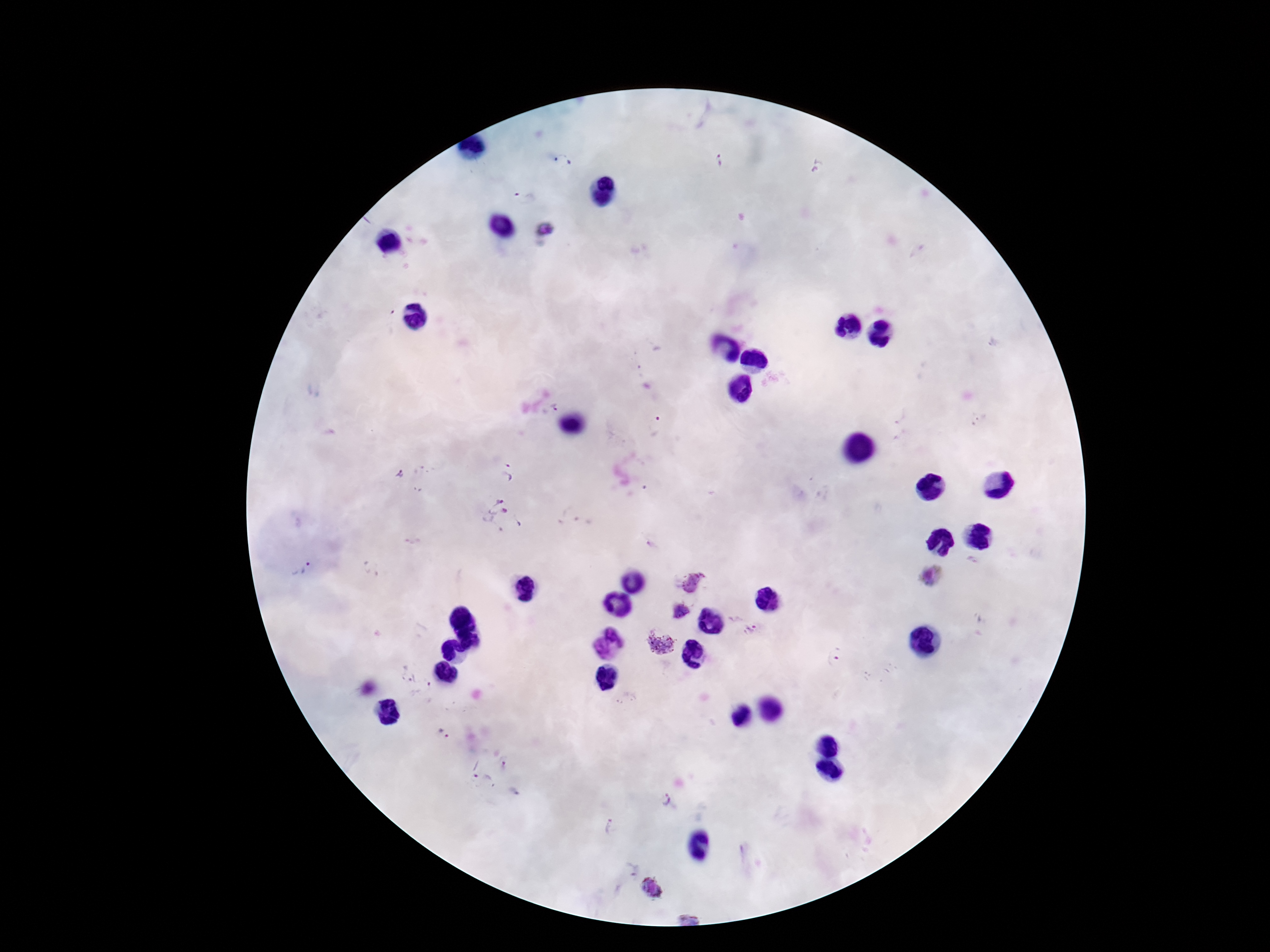
field of view = one from this slide
Plasmodium parasite locations = approximate centers as (x, y) in pixels: (563, 160), (719, 160), (816, 167), (525, 197), (546, 229), (389, 320), (995, 343), (553, 407), (900, 416), (977, 420), (654, 426), (506, 471), (398, 473), (502, 518), (653, 546), (301, 566), (929, 576), (692, 582), (679, 612), (752, 631), (660, 644), (835, 656), (408, 674), (422, 692), (443, 730), (507, 763), (479, 772), (666, 802), (609, 828), (629, 868), (651, 887)
patient malaria status = positive
image size = 1270×952 pixels
capture = smartphone camera through the microscope eyepiece
stain = Giemsa
preparation = thick blood film
magnification = 100x